Classify this cell by malaria status.
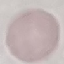

Uninfected.

{
  "preparation": "thin blood film",
  "stain": "Giemsa",
  "capture": "smartphone through the microscope eyepiece",
  "image_type": "cell patch, automatically extracted from a larger field of view and resized to 64 × 64 pixels"
}